Outline each Plasmodium falciparum-infected red blood cell.
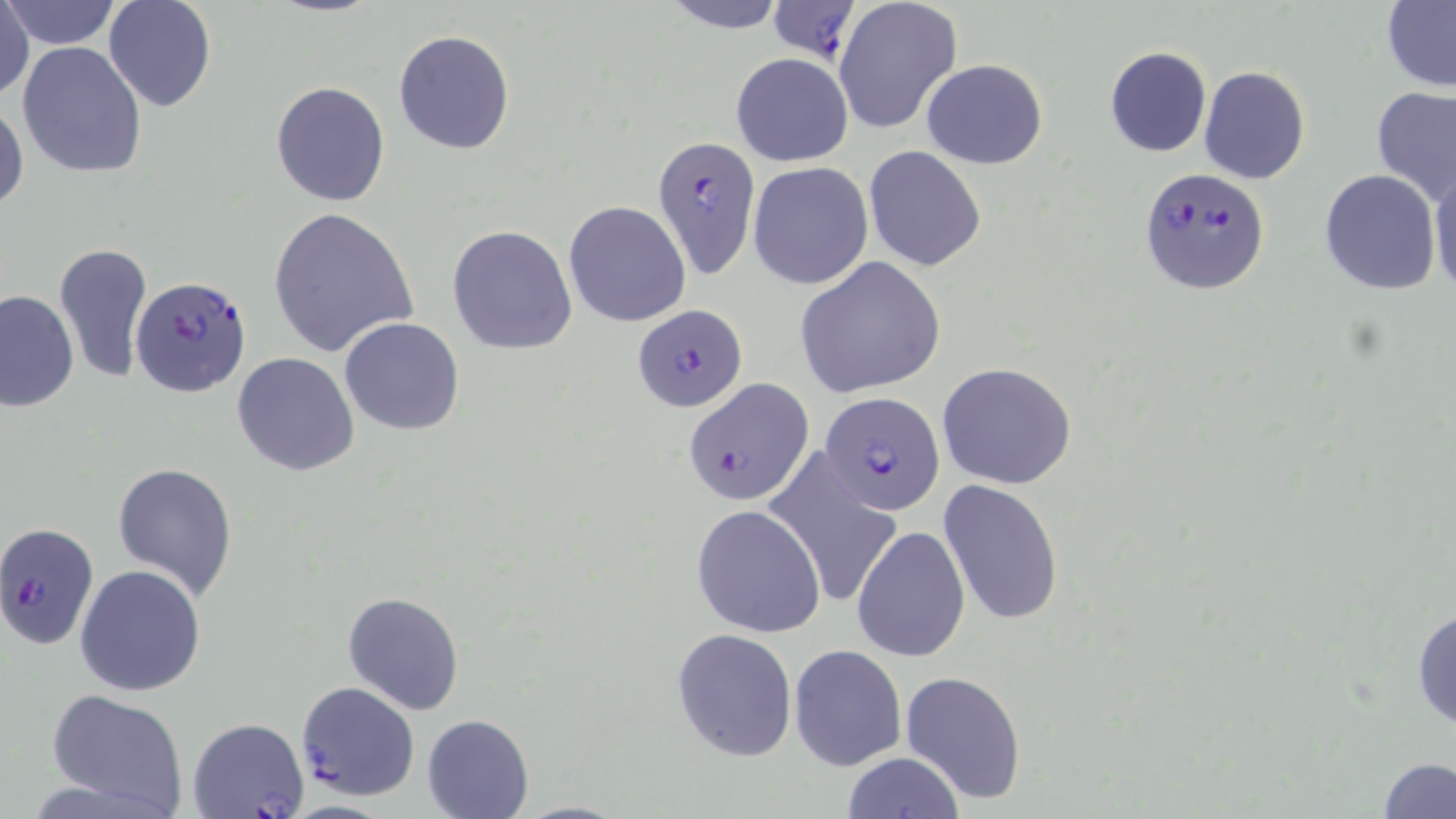

Approximate bounding boxes as [x1, y1, x2, y2] in pixels.
Plasmodium falciparum-infected red blood cells: [767, 0, 859, 63], [653, 134, 761, 279], [1140, 168, 1269, 295], [131, 275, 252, 398], [632, 304, 747, 412], [685, 379, 811, 506], [822, 391, 946, 517], [0, 523, 97, 649], [295, 681, 420, 800], [188, 717, 309, 818].

Summary:
  - Uninfected red blood cell locations: [3, 0, 121, 51], [103, 0, 217, 113], [657, 0, 791, 32], [832, 0, 963, 134], [1381, 1, 1455, 88], [0, 4, 37, 102], [393, 28, 516, 156], [16, 39, 148, 179], [1103, 46, 1213, 157], [730, 53, 853, 167], [921, 59, 1048, 170], [1198, 67, 1310, 184], [271, 80, 390, 207], [1372, 85, 1455, 205], [0, 99, 26, 217], [864, 146, 987, 272], [1429, 158, 1456, 296], [747, 162, 873, 290], [1319, 168, 1442, 295], [563, 200, 692, 326], [266, 206, 417, 356], [448, 225, 578, 355], [53, 243, 152, 384], [795, 256, 945, 399], [2, 290, 78, 412], [339, 317, 467, 436], [232, 352, 361, 476], [937, 362, 1076, 490], [760, 449, 905, 610], [111, 462, 239, 598], [939, 478, 1064, 626], [692, 505, 826, 635], [851, 525, 969, 663], [75, 565, 206, 697], [342, 591, 466, 714], [1411, 602, 1456, 734], [672, 627, 797, 761], [789, 644, 907, 770], [901, 670, 1027, 805], [44, 689, 190, 816], [422, 712, 534, 817], [840, 751, 963, 818], [1375, 755, 1456, 817], [512, 800, 635, 818]
  - Slide-level diagnosis: Plasmodium falciparum
  - Magnification: 1000x
  - Preparation: thin blood film
  - Stain: May-Grünwald-Giemsa
  - Image size: 1456×819 pixels
  - Field of view: single
  - Modality: light microscopy